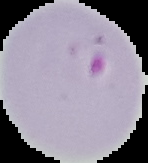

From a thin blood film. Malaria status: parasitized. Segmented cell region on a black background. Image is 148×163 pixels.